Report the malaria status of this cell.
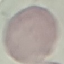
Uninfected.

Summary:
  - Image type: cell patch, automatically extracted from a larger field of view and resized to 64 × 64 pixels
  - Capture: smartphone through the microscope eyepiece
  - Preparation: thin smear
  - Stain: Giemsa